Identify the cell.
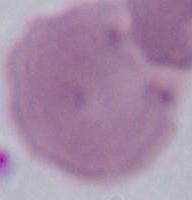
An erythrocyte.

magnification = 1000x
modality = photomicrograph